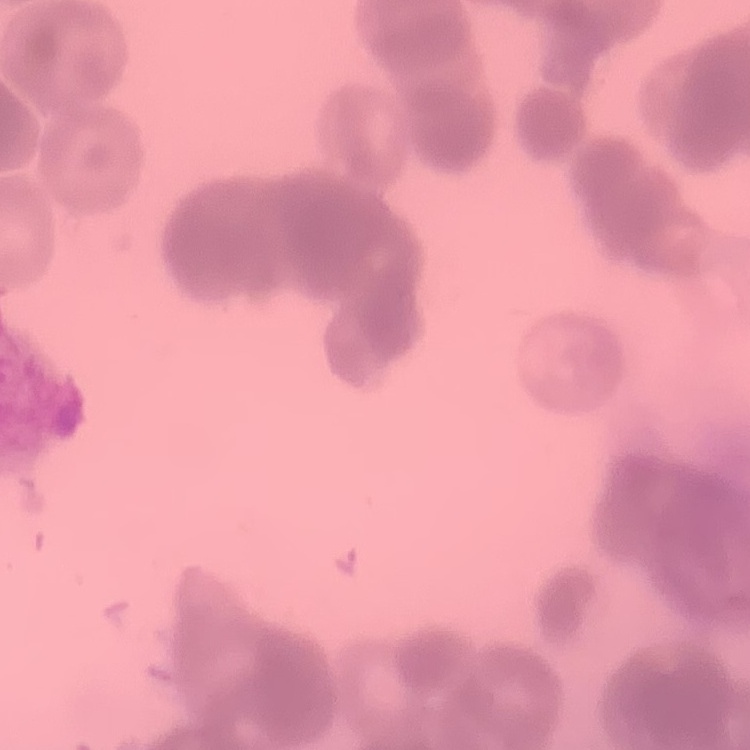

Summary:
  - Red blood cell morphology: rouleaux formation
  - Stain: Field's or Giemsa
  - Image type: square crop of a larger photomicrograph
  - Preparation: thin blood film